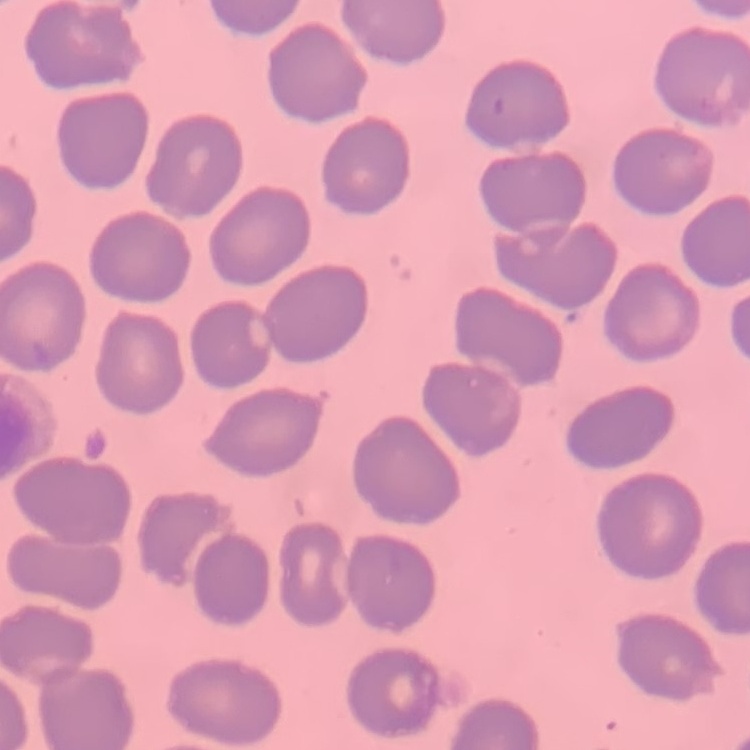
Summary:
  - Erythrocyte morphology: no rouleaux formation
  - Image type: one tile cut from a larger photomicrograph
  - Stain: Field's or Giemsa
  - Preparation: thin blood smear